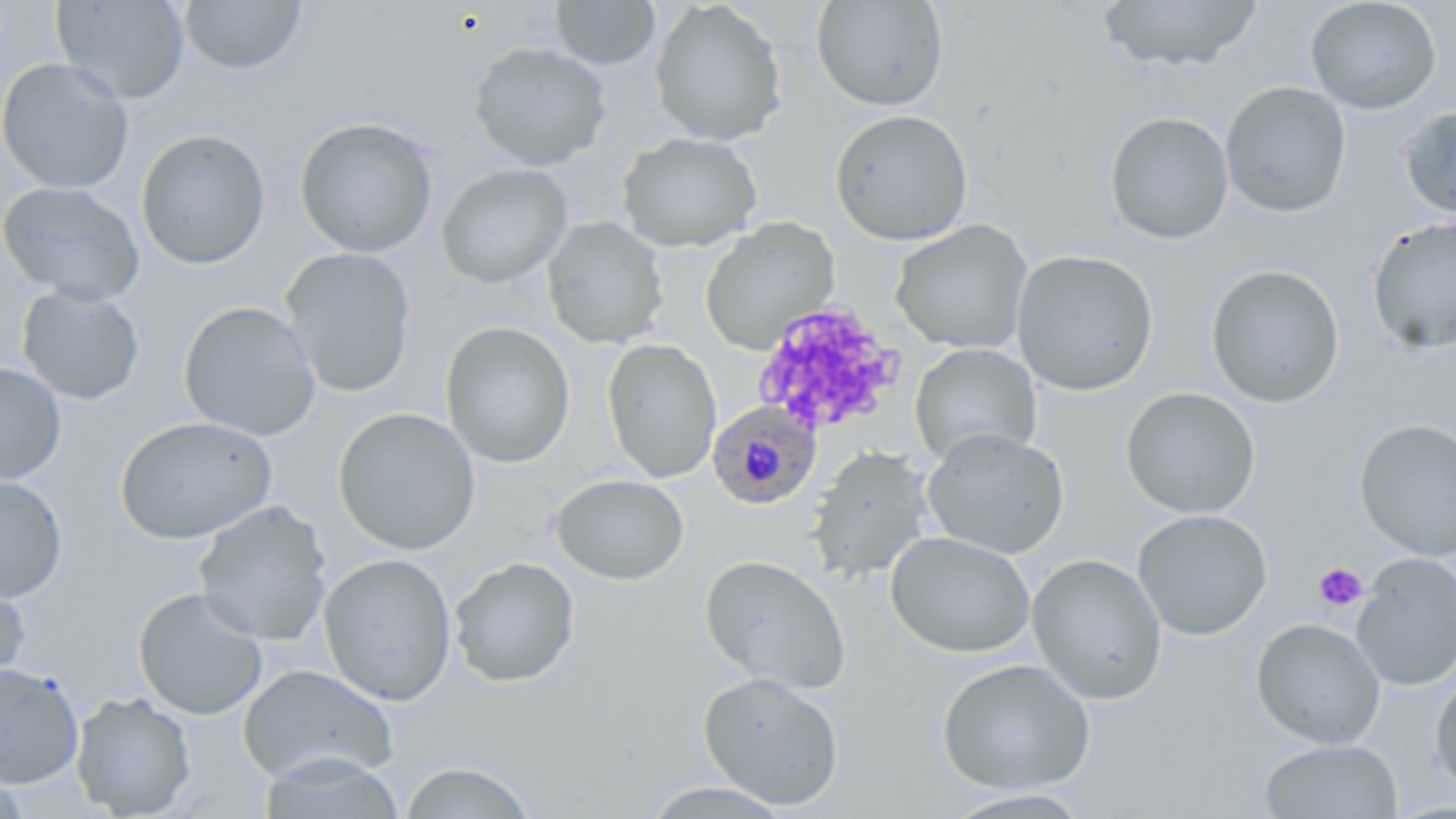

Summary:
  - Coordinate format: approximate bounding boxes as (x1,y1)-(x2,y2) corner pairs in pixels
  - Platelet locations: (751,300)-(904,439), (1313,562)-(1368,612)
  - Uninfected red blood cell locations: (52,0)-(191,105), (179,0)-(308,76), (649,0)-(788,147), (811,0)-(949,112), (1096,0)-(1265,73), (1304,0)-(1442,114), (550,1)-(661,71), (467,42)-(612,172), (0,57)-(134,194), (1220,81)-(1352,218), (1399,104)-(1456,222), (830,109)-(973,246), (1103,111)-(1234,245), (294,116)-(439,258), (135,128)-(272,271), (617,133)-(763,253), (435,164)-(574,289), (0,181)-(145,305), (542,216)-(669,350), (1366,216)-(1456,355), (699,217)-(840,355), (889,220)-(1033,355), (279,247)-(417,397), (1011,248)-(1159,396), (1205,264)-(1346,409), (16,285)-(146,406), (178,300)-(322,442), (440,321)-(576,468), (601,338)-(722,483), (909,344)-(1042,467), (0,361)-(68,486), (1120,387)-(1261,518), (333,407)-(481,556), (114,416)-(277,545), (1354,418)-(1456,560), (921,428)-(1070,560), (807,446)-(933,582), (550,473)-(690,586), (0,475)-(68,603), (193,501)-(333,647), (1132,509)-(1273,641), (884,532)-(1036,658), (318,553)-(457,707), (1026,553)-(1168,705), (699,554)-(851,695), (1351,554)-(1456,691), (448,557)-(581,688), (0,569)-(31,692), (132,587)-(269,720), (1251,618)-(1386,750), (936,658)-(1096,795), (0,662)-(84,788), (237,664)-(399,786), (1430,668)-(1456,800), (697,671)-(846,810), (71,692)-(197,818), (1258,739)-(1402,818), (257,753)-(408,818), (397,761)-(539,818), (638,781)-(794,817), (938,788)-(1097,818)
  - Plasmodium falciparum-infected red blood cell locations: (707,401)-(821,510)
  - Slide-level diagnosis: Plasmodium falciparum
  - Magnification: 1000x
  - Preparation: thin blood film
  - Modality: light microscopy
  - Field of view: single
  - Stain: May-Grünwald-Giemsa
  - Image size: 1456×819 pixels